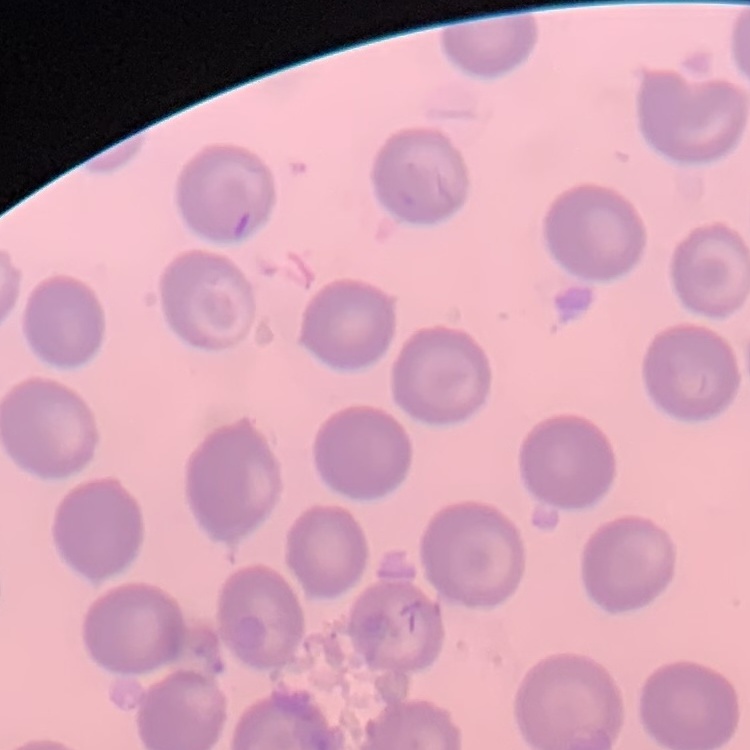

red blood cell morphology = no rouleaux formation
stain = Field's or Giemsa
image type = square crop of a larger photomicrograph
preparation = thin peripheral smear